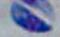

magnification: 1000x
modality: micrograph
identification: Toxoplasma gondii